Outline each blood parasite and name the species.
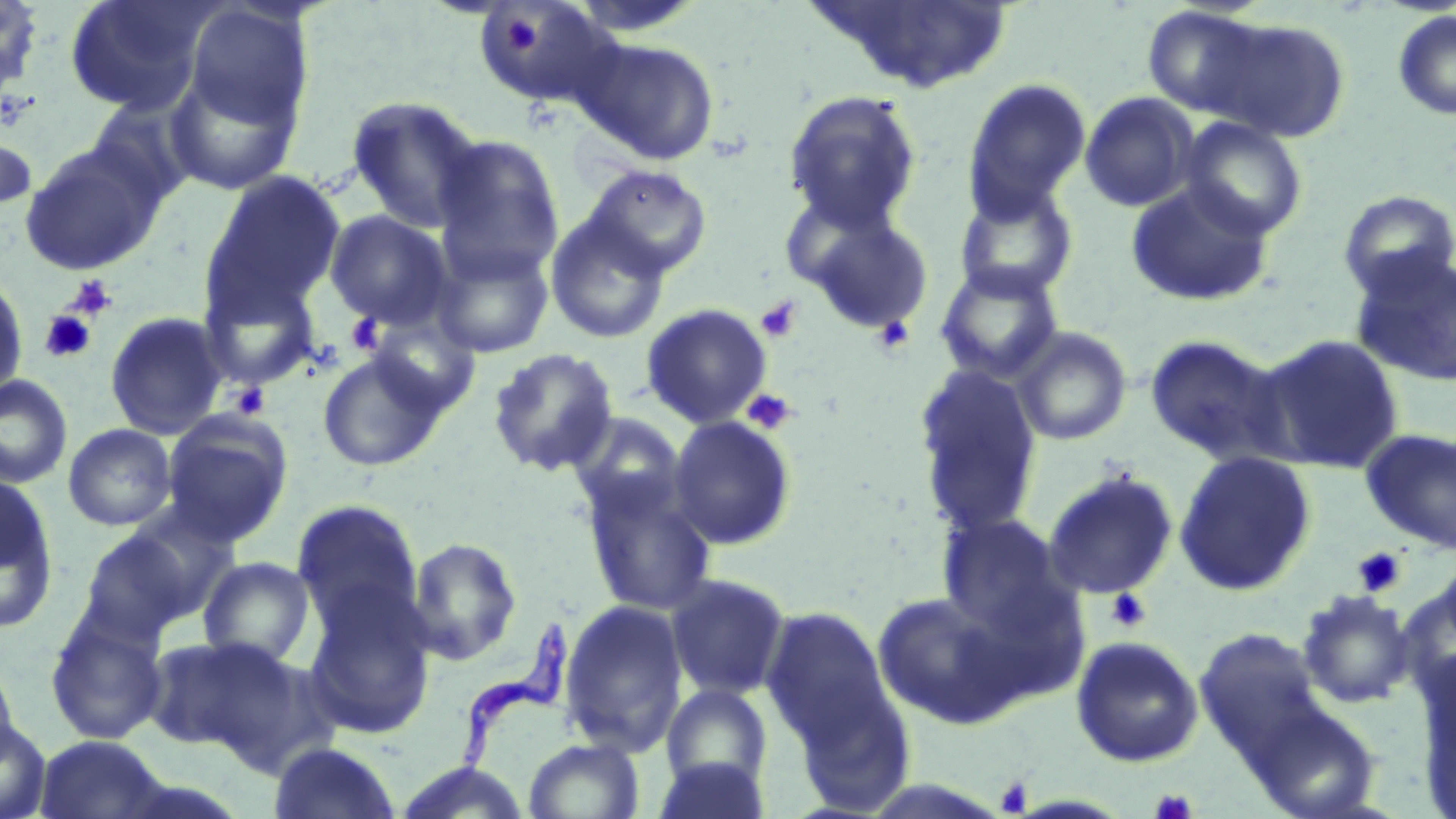
Approximate bounding boxes as [x1, y1, x2, y2] in pixels.
Trypanosoma brucei: [424, 621, 571, 805].
No Plasmodium falciparum, Plasmodium ovale, Plasmodium malariae, Plasmodium vivax, or Babesia divergens observed.

slide_level_diagnosis: Trypanosoma brucei
platelet_locations: 'approximate bounding boxes as [x1, y1, x2, y2] in pixels: [502, 17, 543, 56], [68, 275, 117, 320], [756, 297, 802, 343], [38, 309, 98, 364], [345, 313, 386, 356], [872, 314, 915, 354], [231, 382, 270, 420], [740, 388, 798, 435], [1352, 547, 1408, 597], [1105, 587, 1152, 634], [995, 777, 1034, 816], [1150, 787, 1197, 819]'
modality: optical microscopy
field_of_view: one of a larger specimen
stain: May-Grünwald-Giemsa
preparation: thin blood film
image_size: 1456×819 pixels
magnification: 1000x
uninfected_red_blood_cell_locations: 'approximate bounding boxes as [x1, y1, x2, y2] in pixels: [0, 0, 44, 101], [64, 0, 216, 115], [804, 0, 1016, 95], [474, 2, 623, 111], [183, 3, 313, 132], [1140, 5, 1274, 121], [1392, 9, 1456, 121], [1199, 16, 1351, 143], [574, 36, 721, 166], [161, 66, 304, 196], [962, 78, 1092, 221], [782, 89, 922, 233], [1079, 91, 1199, 212], [346, 94, 486, 234], [1178, 116, 1309, 240], [0, 128, 37, 220], [431, 135, 565, 282], [19, 144, 164, 275], [584, 164, 713, 279], [201, 171, 348, 322], [1125, 181, 1276, 308], [953, 182, 1079, 301], [1337, 189, 1456, 301], [796, 206, 935, 335], [324, 210, 454, 331], [544, 215, 671, 344], [429, 241, 555, 358], [1349, 250, 1456, 387], [935, 261, 1065, 384], [0, 271, 28, 408], [200, 275, 323, 390], [640, 303, 773, 429], [104, 311, 230, 440], [363, 315, 482, 419], [1011, 326, 1132, 446], [1253, 333, 1406, 475], [1144, 334, 1291, 468], [487, 347, 620, 478], [316, 351, 448, 473], [912, 366, 1044, 535], [0, 374, 74, 489], [667, 416, 797, 550], [161, 417, 292, 546], [63, 423, 177, 531], [1360, 427, 1456, 556], [1173, 450, 1317, 597], [1042, 468, 1179, 600], [579, 472, 718, 618], [0, 474, 60, 634], [290, 499, 425, 638], [937, 513, 1076, 638], [76, 523, 211, 642], [407, 537, 522, 666], [197, 556, 317, 668], [665, 573, 792, 701], [300, 583, 437, 739], [873, 589, 1029, 728], [1297, 589, 1415, 708], [559, 600, 689, 756], [761, 606, 894, 749], [44, 610, 169, 746], [1193, 628, 1335, 771], [144, 635, 296, 756], [1070, 635, 1204, 767], [0, 654, 21, 769], [660, 684, 774, 793], [0, 717, 51, 819], [34, 735, 173, 819], [523, 738, 645, 819], [268, 741, 402, 819], [653, 755, 770, 819], [390, 762, 535, 818]'